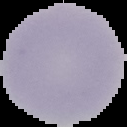 Malaria status: uninfected. From a thin blood smear. Image is 127×127 pixels. The area outside the segmented cell region is set to black.